Classify this cell by malaria status.
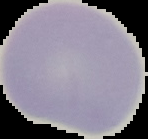

It is uninfected.

Summary:
  - Preparation: thin blood film
  - Image type: segmented cell region with the area outside set to black
  - Image size: 148×139 pixels